Identify the parasite.
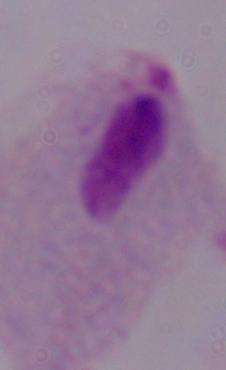

This is a trichomonad.

modality = photomicrograph
magnification = 1000x